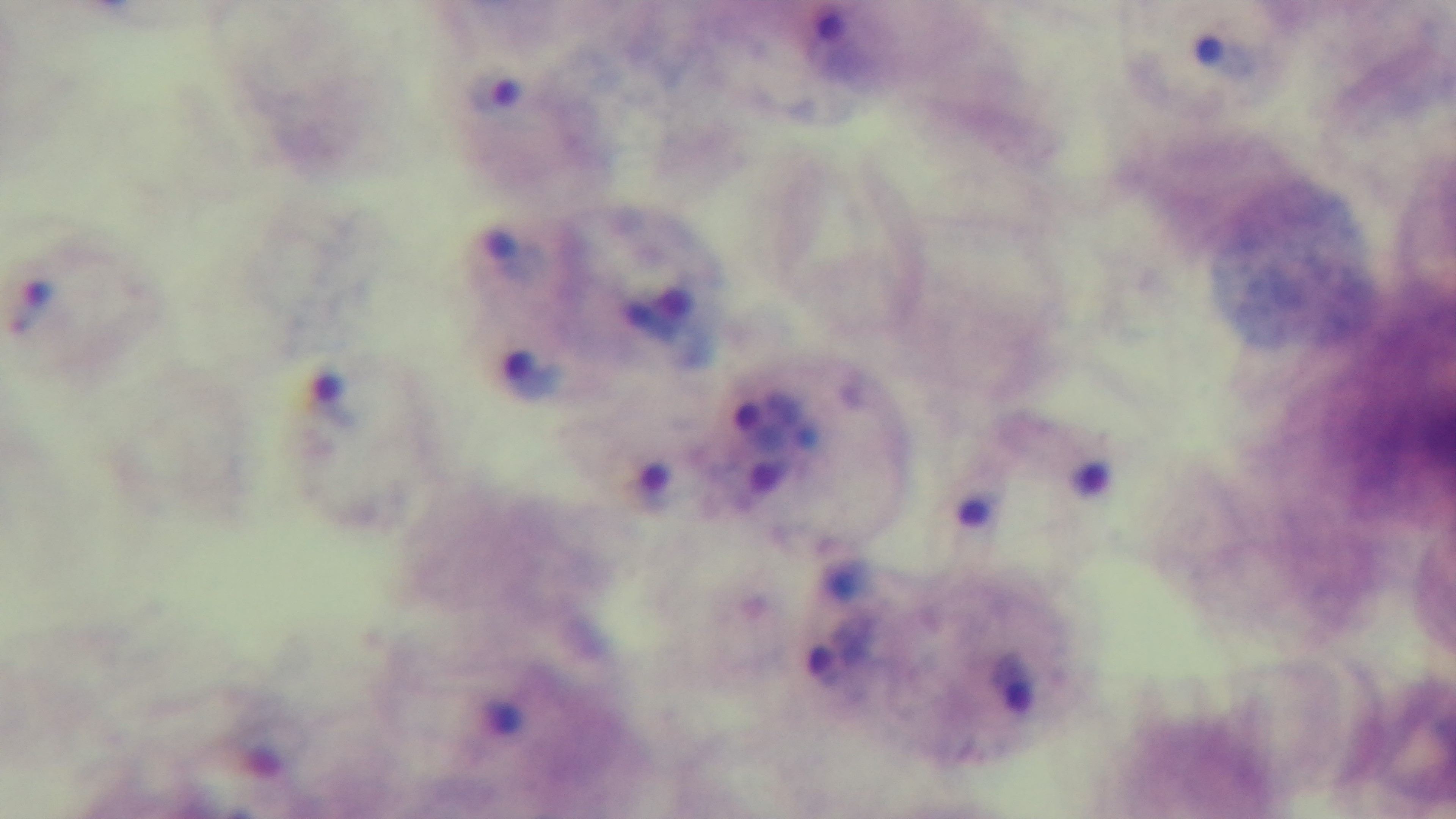

Summary:
  - Malaria status: infected
  - Field of view: single
  - Modality: light microscopy
  - Preparation: thick blood film
  - Objective: 100x oil immersion
  - Stain: Giemsa
  - Capture: mounted 4K digital camera